Describe the morphology of the erythrocytes.
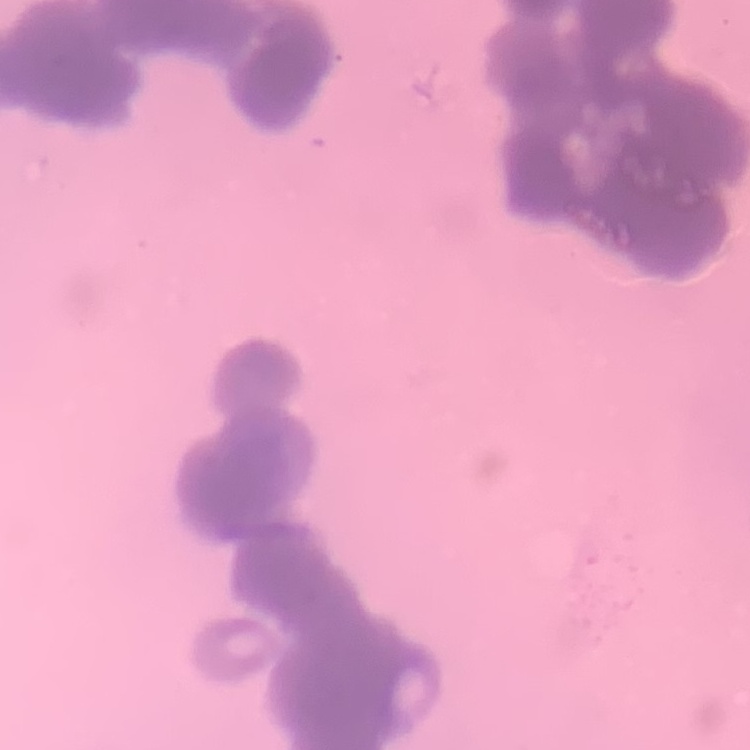
Rouleaux formation.

Thin blood film. One tile cut from a larger photomicrograph. Field's or Giemsa stain.